Locate every Plasmodium parasite.
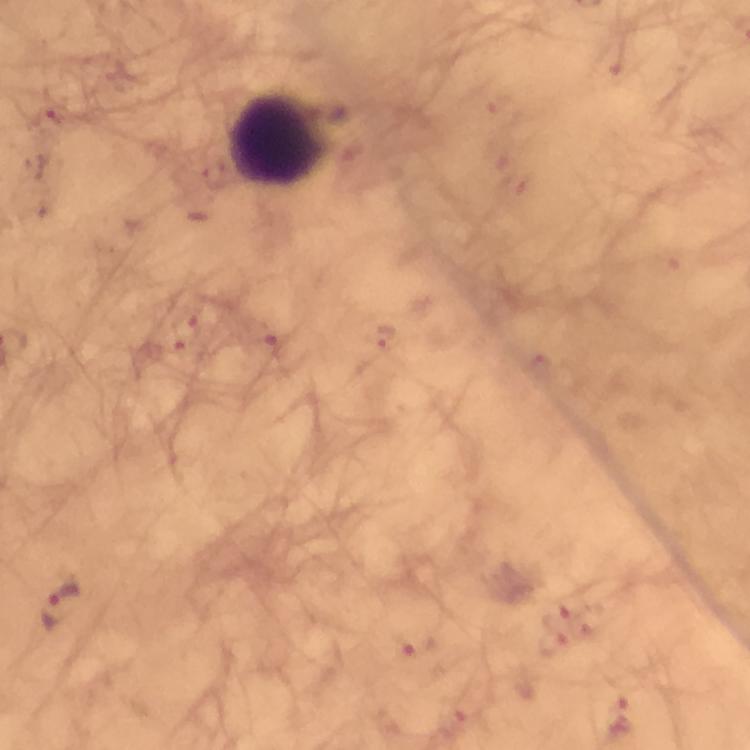

Approximate centers as (x, y) in pixels.
Plasmodium parasites: (51, 117), (187, 331), (384, 339), (269, 340), (62, 604), (556, 616), (417, 647), (554, 647), (619, 715), (453, 724).

Leukocyte locations: (279, 141). Cropped region of a single field of view. Image is 750×750 pixels. Thick smear. Photographed with a smartphone mounted on the microscope. Immersion oil was used. Giemsa-stained preparation. From a diagnostic examination for malaria. At 100x magnification.